Point out each Plasmodium parasite and each leukocyte.
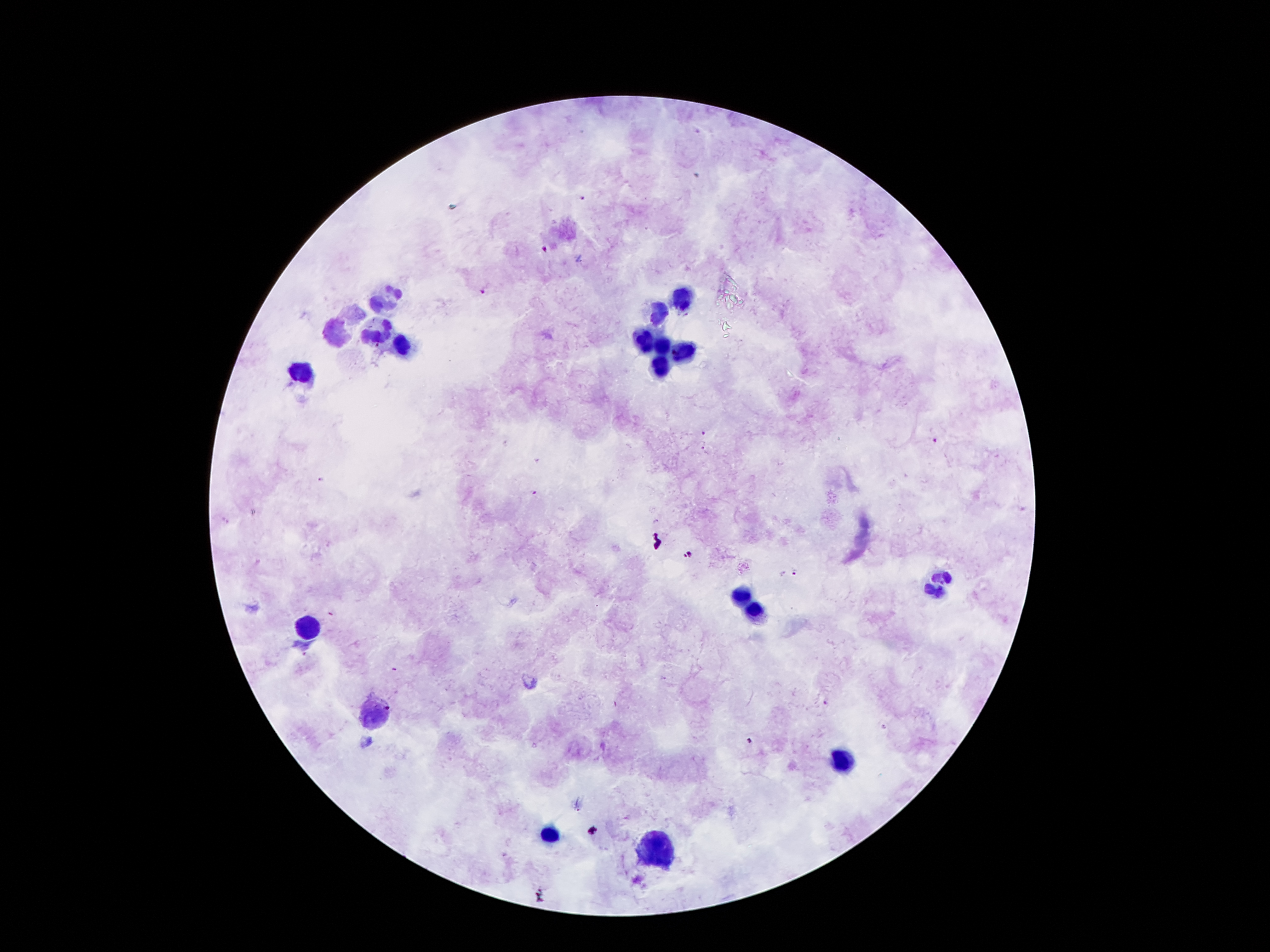

Approximate centers as (x, y) in pixels.
Plasmodium parasites: (582, 198), (543, 250), (483, 291), (703, 433), (936, 440), (704, 448), (323, 480), (533, 492), (227, 521), (655, 522), (797, 572), (782, 574), (826, 704), (749, 742).
Leukocytes: (383, 298), (681, 298), (656, 314), (381, 330), (338, 332), (641, 340), (662, 346), (399, 347), (679, 350), (660, 365), (303, 371), (938, 584), (740, 595), (755, 612), (308, 626), (371, 711), (842, 758), (551, 834), (651, 847).

image_size: 1270×952 pixels
capture: smartphone through the microscope eyepiece
magnification: 100x
field_of_view: single
stain: Giemsa
patient_malaria_status: infected with Plasmodium falciparum
preparation: thick blood film